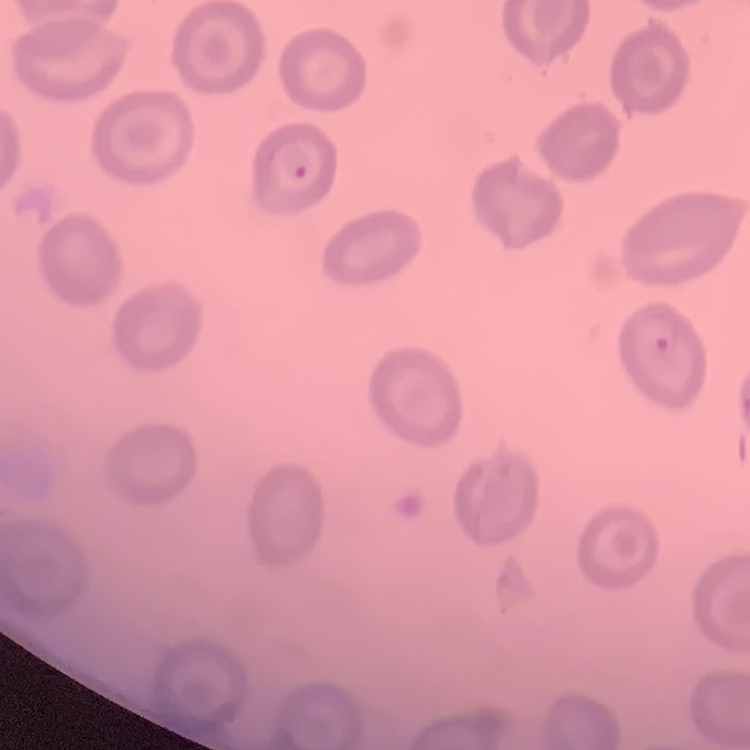

erythrocyte morphology = no rouleaux formation
stain = Field's or Giemsa
preparation = thin blood smear
image type = square crop of a larger photomicrograph